Locate every blood parasite and identify its species.
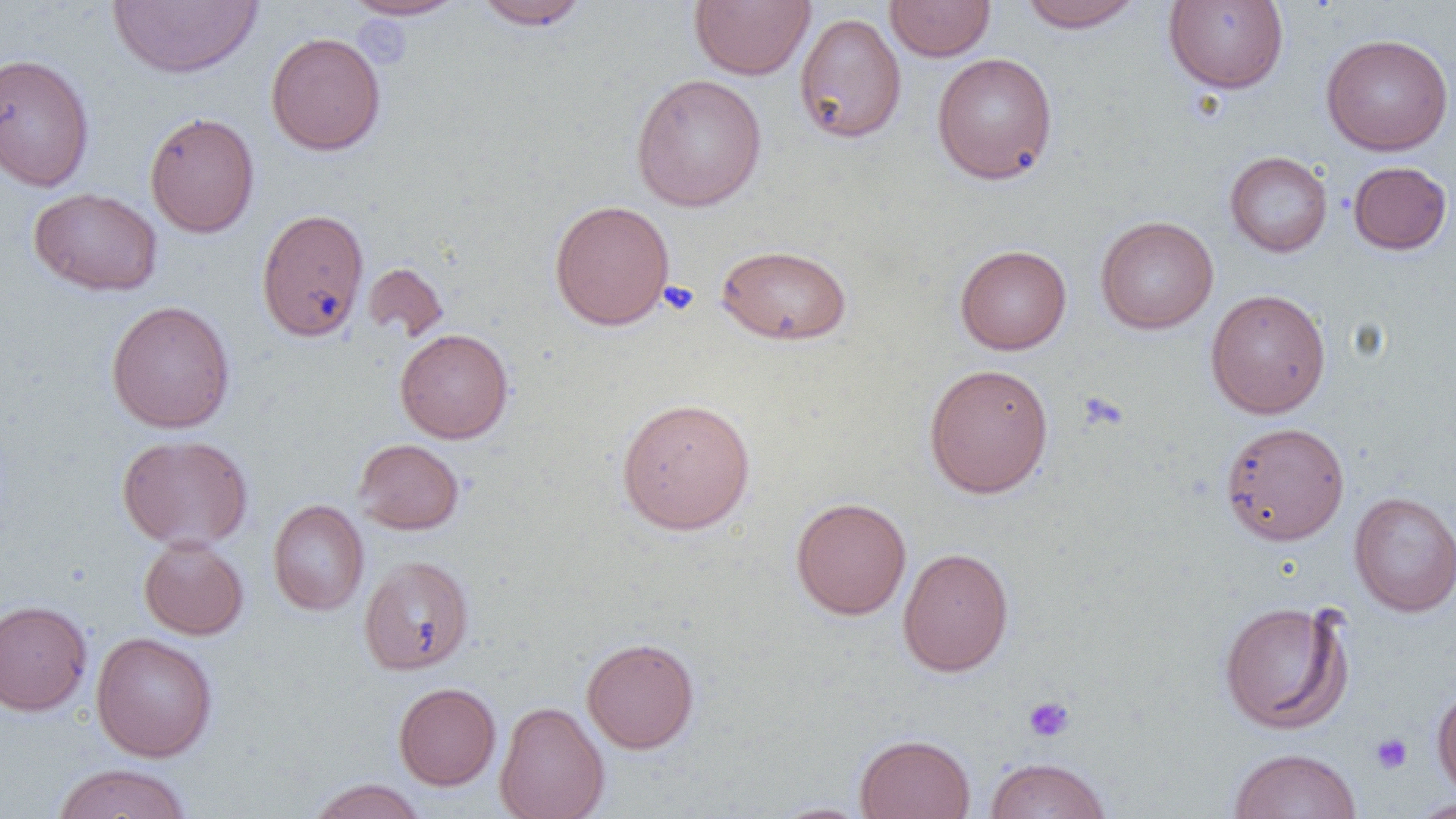
No blood parasites seen.

Approximate bounding boxes as (x1, y1, x2, y2) in pixels. Uninfected red blood cell locations: (342, 0, 468, 21), (689, 0, 815, 80), (885, 0, 996, 61), (1017, 0, 1146, 33), (108, 1, 261, 79), (473, 1, 590, 31), (1163, 1, 1289, 93), (794, 12, 907, 144), (266, 32, 386, 155), (1321, 33, 1453, 156), (0, 52, 95, 191), (931, 52, 1058, 184), (630, 72, 767, 211), (145, 111, 260, 237), (1224, 151, 1333, 257), (1348, 161, 1452, 255), (28, 187, 163, 296), (548, 199, 675, 330), (256, 208, 369, 342), (1095, 215, 1218, 334), (716, 244, 852, 345), (955, 244, 1072, 354), (362, 262, 449, 342), (1205, 288, 1332, 419), (106, 300, 236, 433), (394, 328, 513, 443), (923, 363, 1054, 498), (616, 396, 756, 535), (1220, 421, 1349, 545), (116, 433, 254, 551), (353, 438, 465, 535), (1349, 490, 1456, 617), (790, 496, 912, 620), (267, 499, 369, 616), (138, 536, 249, 640), (897, 547, 1014, 676), (359, 555, 474, 675), (0, 599, 92, 716), (1218, 599, 1353, 734), (91, 631, 217, 762), (581, 636, 700, 753), (393, 682, 501, 790), (1431, 686, 1456, 797), (495, 700, 610, 819), (855, 733, 976, 819), (1228, 747, 1362, 819), (984, 756, 1112, 819), (50, 762, 195, 819), (306, 778, 427, 819), (1406, 798, 1456, 818), (766, 801, 874, 818). Platelet locations: (659, 280, 700, 316), (1078, 392, 1126, 432), (1023, 696, 1075, 742), (1371, 733, 1412, 774). Slide-level diagnosis: no evidence of blood parasites. Image is 1456×819 pixels. One field of a larger specimen. Thin blood film. Light microscopy. Captured at 1000x magnification.